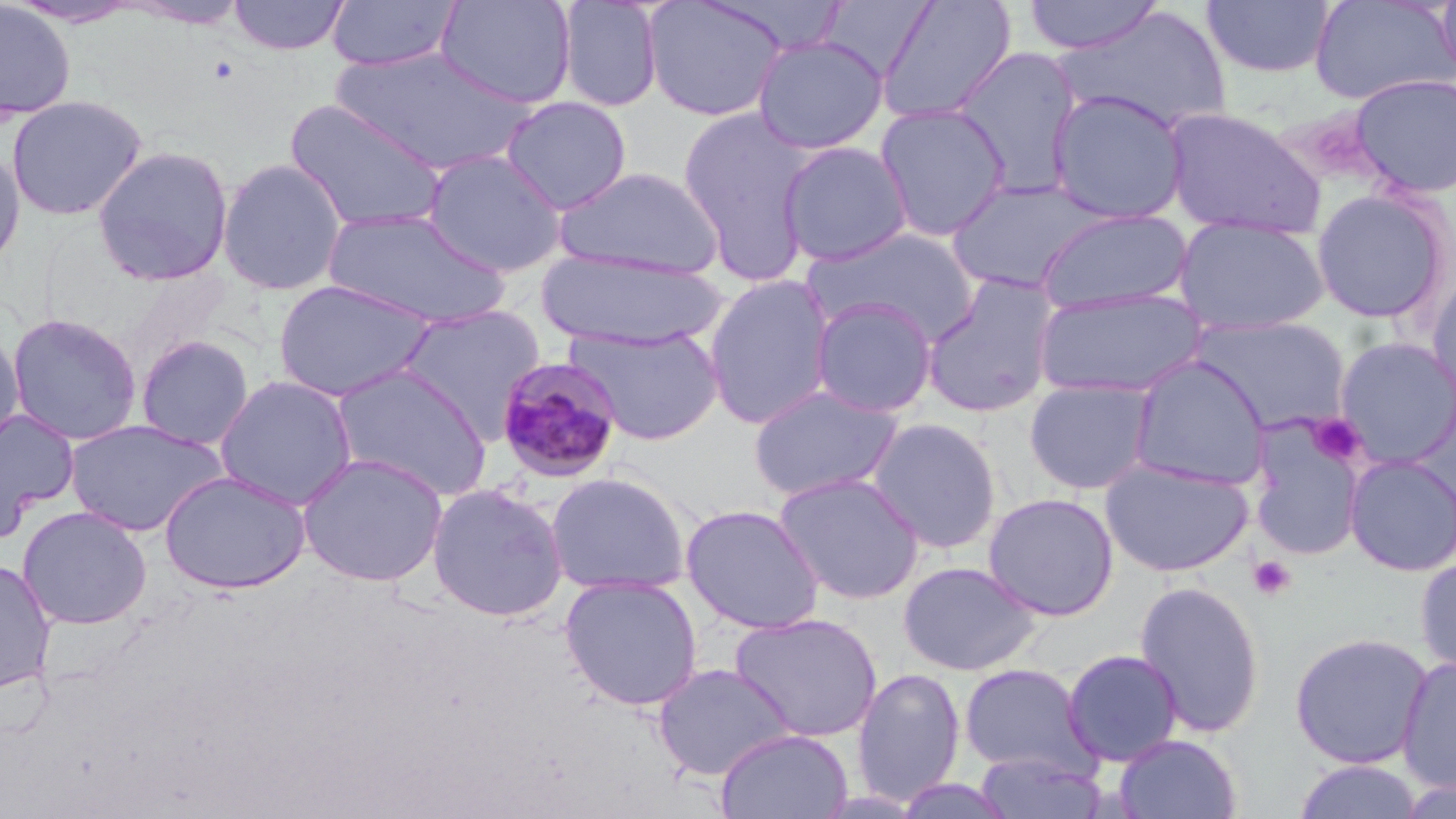 Approximate bounding boxes as [x1, y1, x2, y2] in pixels. Platelet locations: [1308, 414, 1366, 468], [1248, 555, 1297, 601]. Uninfected red blood cell locations: [7, 0, 145, 28], [122, 0, 252, 28], [228, 0, 351, 56], [326, 0, 461, 73], [435, 0, 577, 110], [556, 0, 664, 112], [641, 0, 789, 122], [1023, 0, 1165, 56], [1433, 0, 1456, 88], [0, 1, 77, 121], [876, 1, 1017, 125], [1201, 1, 1336, 79], [1308, 1, 1454, 106], [818, 2, 939, 81], [1055, 5, 1231, 134], [752, 35, 889, 155], [331, 46, 533, 175], [951, 46, 1086, 196], [1349, 74, 1456, 199], [1046, 89, 1191, 224], [6, 93, 148, 221], [501, 95, 632, 214], [284, 98, 448, 234], [873, 102, 1011, 242], [1160, 105, 1326, 240], [677, 106, 818, 283], [778, 141, 913, 267], [0, 144, 27, 276], [91, 145, 234, 287], [421, 149, 567, 278], [217, 158, 348, 296], [556, 166, 725, 279], [946, 178, 1104, 294], [1311, 188, 1453, 324], [1035, 206, 1193, 315], [322, 207, 511, 328], [1174, 215, 1328, 336], [803, 226, 980, 345], [535, 248, 729, 350], [1425, 267, 1456, 411], [921, 273, 1062, 419], [703, 274, 837, 429], [271, 278, 437, 403], [1033, 285, 1208, 399], [810, 297, 938, 418], [396, 304, 547, 440], [6, 312, 143, 445], [1191, 315, 1351, 435], [566, 323, 724, 446], [0, 329, 24, 453], [135, 334, 255, 450], [1333, 336, 1456, 469], [1127, 355, 1273, 491], [330, 363, 493, 501], [215, 375, 358, 510], [1023, 377, 1158, 495], [747, 383, 905, 503], [0, 408, 79, 537], [866, 416, 1003, 554], [63, 418, 228, 537], [1248, 422, 1367, 563], [296, 452, 449, 588], [1344, 454, 1456, 576], [1100, 458, 1253, 577], [159, 470, 312, 594], [545, 471, 692, 596], [772, 471, 926, 605], [425, 482, 569, 622], [982, 492, 1119, 621], [680, 503, 825, 634], [17, 506, 152, 630], [1415, 554, 1456, 679], [0, 559, 57, 694], [896, 561, 1042, 676], [559, 574, 704, 712], [1133, 579, 1266, 739], [729, 612, 883, 742], [1290, 631, 1433, 768], [1061, 649, 1184, 767], [1396, 655, 1456, 793], [653, 662, 794, 781], [958, 662, 1095, 777], [851, 666, 965, 808], [715, 727, 853, 819], [1113, 733, 1243, 819], [972, 748, 1107, 818], [1290, 759, 1425, 819], [892, 776, 1017, 818]. Plasmodium malariae-infected red blood cell locations: [497, 356, 627, 483]. Slide-level diagnosis: Plasmodium malariae. Thin blood smear. One field of a larger specimen. Captured at 1000x magnification. May-Grünwald-Giemsa stain. Optical microscopy. Image is 1456×819 pixels.